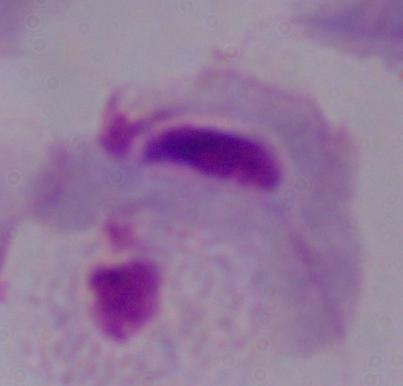 Photomicrograph. 1000x magnification. A trichomonad is shown.